Point out each Plasmodium parasite and each leukocyte.
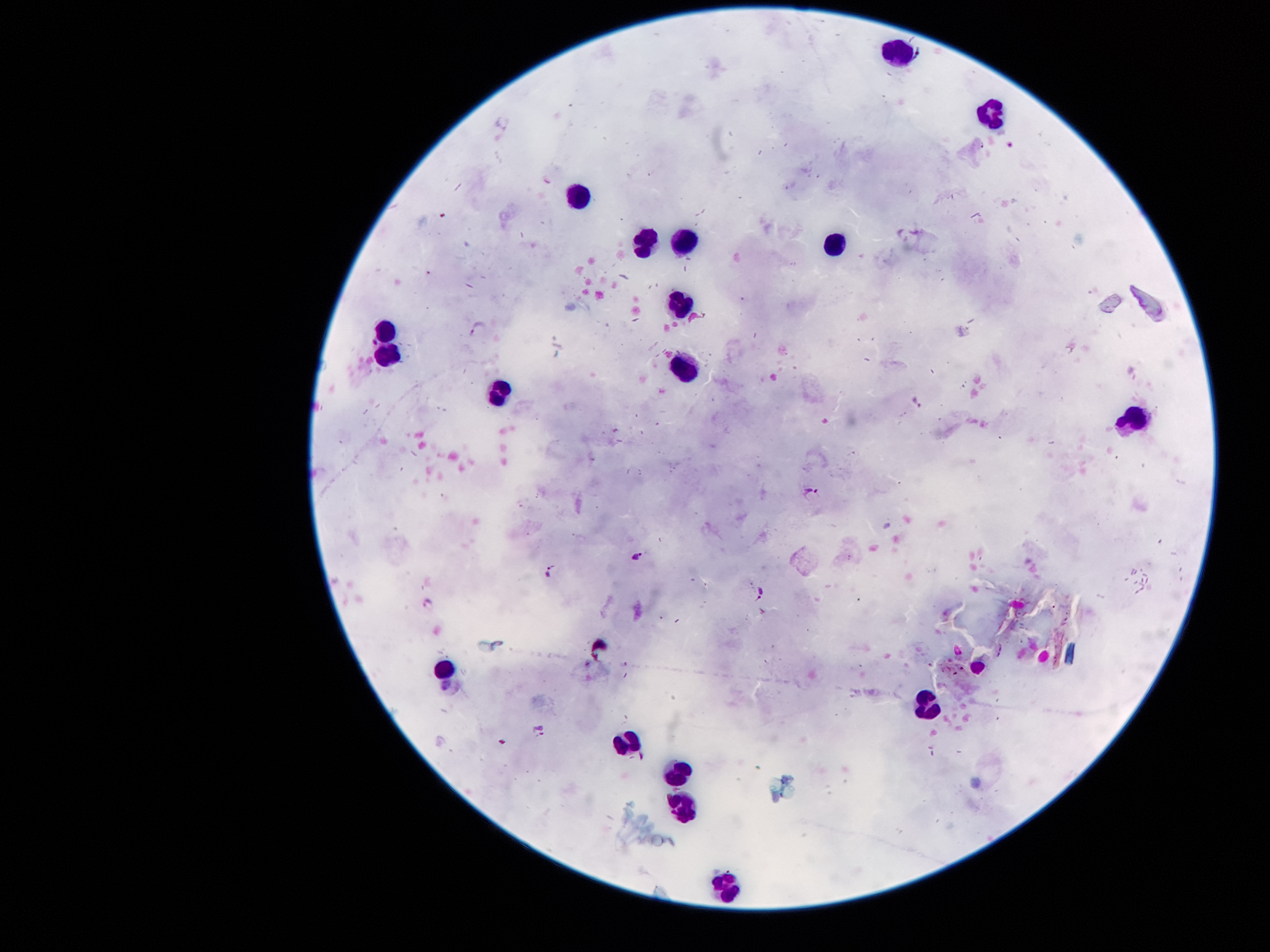

Approximate centers as (x, y) in pixels.
Plasmodium parasites: (920, 56), (479, 328), (372, 343), (919, 404), (813, 496), (635, 555), (549, 572), (762, 592), (428, 604), (538, 729).
Leukocytes: (897, 49), (990, 119), (580, 201), (680, 243), (645, 245), (833, 245), (679, 309), (383, 331), (386, 356), (687, 371), (501, 391), (1138, 419), (441, 667), (928, 707), (629, 741), (679, 775), (687, 807), (727, 887).

magnification = 100x
field of view = one from this slide
capture = smartphone camera through the microscope eyepiece
stain = Giemsa
preparation = thick blood film
image size = 1270×952 pixels
patient malaria status = infected with Plasmodium falciparum